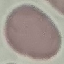
Malaria status: uninfected. Automatically extracted cell patch, resized to 64 × 64 pixels. Photographed with a smartphone camera at the microscope eyepiece. Giemsa-stained preparation. Thin blood film.